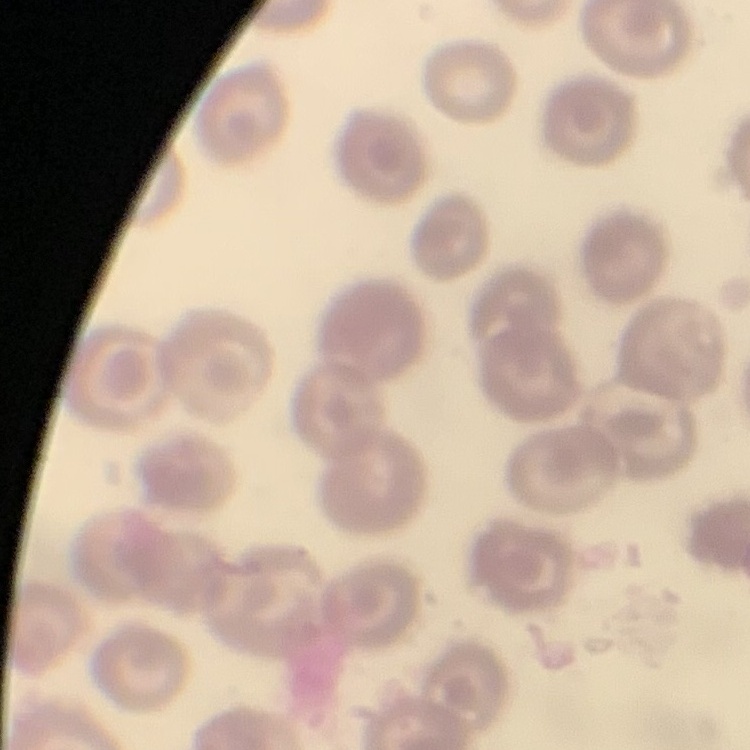 The red blood cells show no rouleaux formation. Thin blood smear. Field's or Giemsa stain. Square crop of a larger photomicrograph.